Assess the morphology of the erythrocytes.
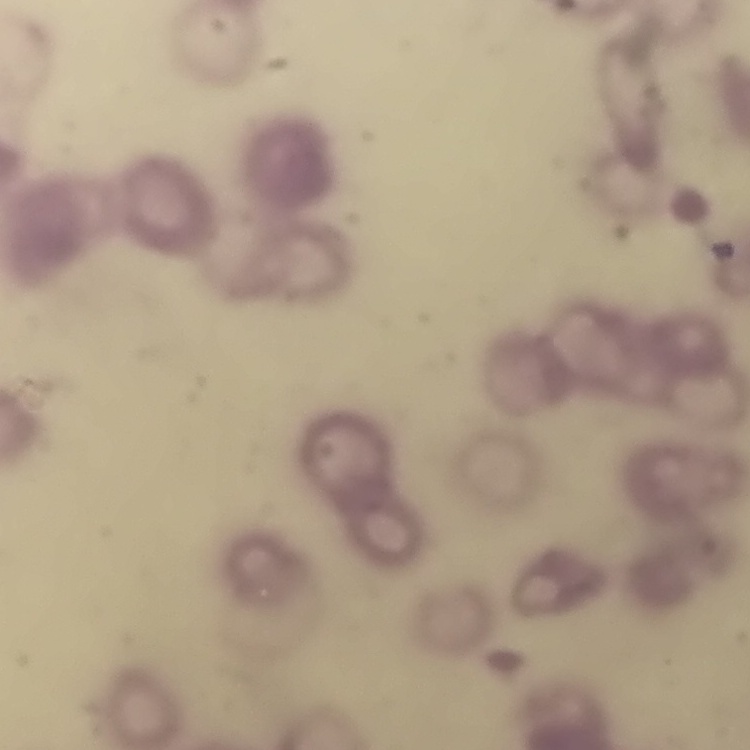

Rouleaux formation.

Field's or Giemsa stain. One tile cut from a larger photomicrograph. Thin peripheral smear.